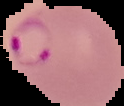

image type = segmented cell region on a black background
image size = 124×106 pixels
preparation = thin blood smear
result = Plasmodium parasites detected